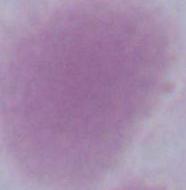

A red blood cell is shown. 1000x magnification. Photomicrograph.